Name the parasite shown.
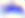
Toxoplasma gondii.

Summary:
  - Magnification: 400x
  - Modality: micrograph